Locate every blood parasite and identify its species.
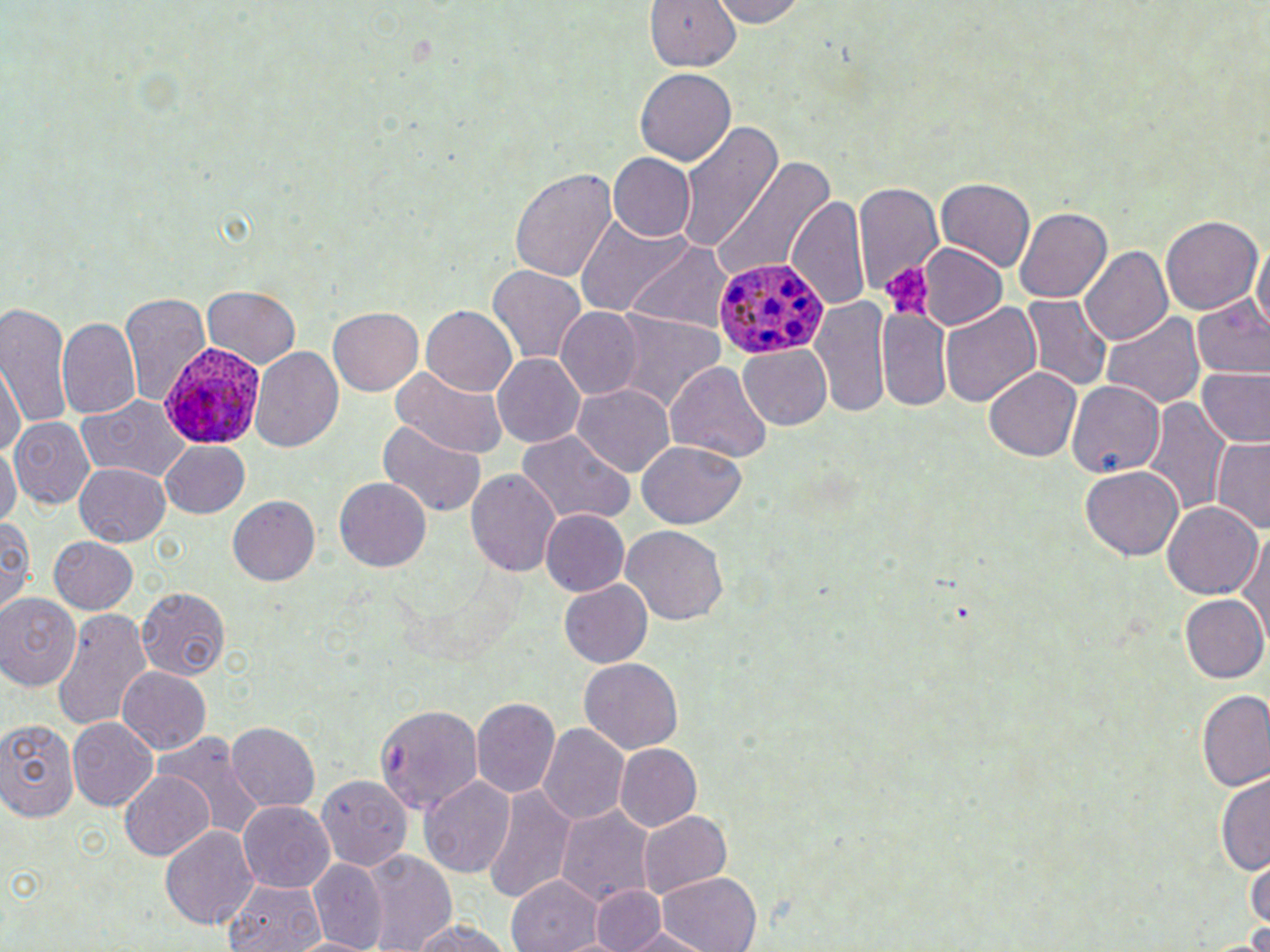

Approximate bounding boxes as [x1, y1, x2, y2] in pixels.
Plasmodium ovale-infected red blood cells: [714, 257, 827, 361], [160, 340, 264, 446].
No Plasmodium falciparum, Plasmodium malariae, Plasmodium vivax, Babesia divergens, or Trypanosoma brucei observed.

slide-level diagnosis = Plasmodium ovale
magnification = 1000x
modality = light microscopy
stain = May-Grünwald-Giemsa
platelet locations = approximate bounding boxes as [x1, y1, x2, y2] in pixels: [881, 263, 935, 321]
image size = 1270×952 pixels
field of view = single
preparation = thin blood film
uninfected red blood cell locations = approximate bounding boxes as [x1, y1, x2, y2] in pixels: [645, 0, 740, 70], [710, 0, 807, 27], [635, 68, 736, 167], [677, 119, 780, 260], [608, 153, 696, 241], [713, 157, 835, 281], [510, 168, 618, 283], [935, 177, 1036, 272], [851, 180, 944, 293], [787, 195, 872, 312], [1016, 209, 1112, 302], [1160, 214, 1263, 314], [575, 215, 693, 315], [1251, 238, 1270, 337], [623, 240, 732, 334], [917, 242, 1008, 330], [1079, 245, 1173, 345], [488, 265, 586, 365], [204, 285, 301, 366], [118, 294, 213, 408], [1022, 296, 1113, 390], [1194, 297, 1270, 379], [813, 298, 891, 418], [1, 302, 73, 430], [940, 302, 1040, 409], [422, 305, 518, 397], [556, 307, 642, 399], [876, 307, 952, 412], [329, 308, 422, 394], [606, 309, 724, 411], [1099, 311, 1204, 409], [56, 316, 143, 419], [740, 345, 831, 429], [249, 346, 343, 453], [491, 353, 586, 448], [1, 358, 24, 453], [665, 362, 771, 462], [1198, 366, 1269, 447], [983, 367, 1082, 462], [391, 369, 511, 459], [1066, 380, 1166, 478], [573, 383, 676, 478], [76, 396, 194, 481], [1145, 399, 1229, 515], [9, 416, 94, 508], [376, 421, 486, 517], [514, 429, 636, 525], [0, 438, 21, 531], [1211, 438, 1270, 532], [637, 440, 746, 528], [160, 441, 250, 517], [74, 462, 170, 545], [1081, 466, 1183, 560], [465, 469, 562, 578], [334, 477, 432, 572], [228, 495, 320, 585], [1163, 501, 1263, 599], [540, 509, 629, 595], [0, 515, 35, 613], [620, 525, 729, 626], [1235, 529, 1269, 643], [48, 537, 139, 614], [560, 580, 652, 668], [136, 587, 230, 679], [0, 594, 82, 690], [1180, 594, 1269, 684], [52, 607, 152, 729], [580, 658, 682, 752], [117, 665, 211, 753], [125, 671, 227, 815], [1198, 690, 1269, 790], [470, 696, 561, 799], [372, 699, 514, 811], [68, 717, 158, 810], [0, 719, 80, 822], [227, 721, 321, 813], [537, 723, 631, 823], [157, 735, 261, 841], [615, 744, 702, 829], [121, 770, 213, 861], [1216, 771, 1270, 874], [311, 775, 412, 875], [418, 775, 515, 879], [484, 786, 575, 904], [238, 801, 335, 893], [555, 804, 656, 904], [638, 812, 732, 897], [159, 826, 259, 929], [360, 848, 457, 952], [1246, 858, 1269, 932], [309, 859, 385, 949], [656, 872, 761, 951], [507, 875, 604, 952], [224, 880, 321, 952], [589, 886, 666, 951], [407, 917, 513, 952], [617, 927, 713, 951], [288, 936, 376, 952]